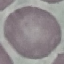

Malaria status: uninfected. Giemsa-stained preparation. Photographed with a smartphone camera at the microscope eyepiece. Cell patch, automatically extracted from a larger field of view and resized to 64 × 64 pixels. Thin smear of blood.